Classify this cell by malaria status.
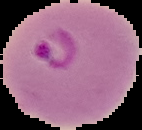

It is parasitized.

Segmented cell region on a black background. Image is 142×130 pixels. From a thin blood film.